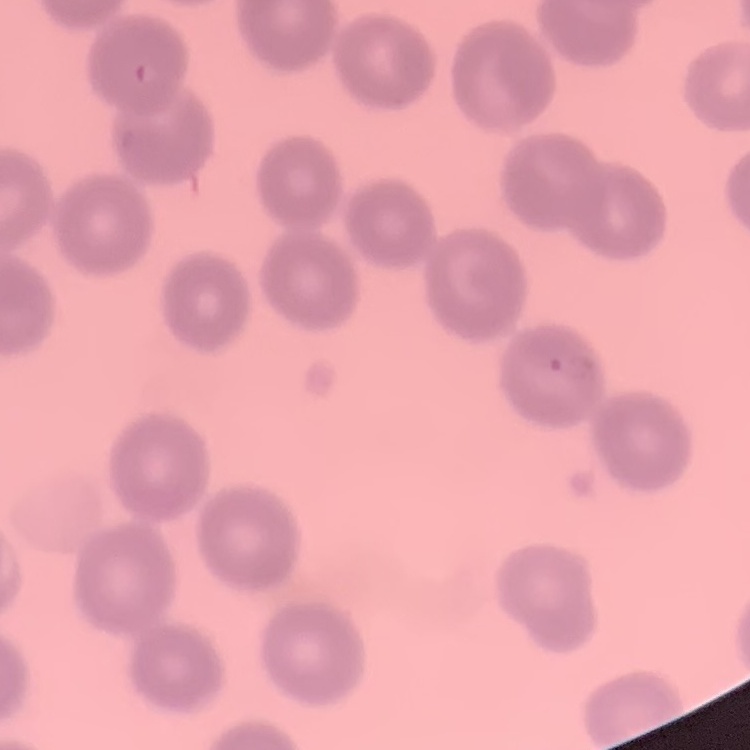 The red blood cells exhibit no rouleaux formation. Thin peripheral smear. Square crop of a larger photomicrograph. Stained with either Field's or Giemsa.